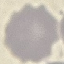

Summary:
  - Malaria status: uninfected
  - Stain: Giemsa
  - Image type: cell patch, automatically extracted from a larger field of view and resized to 64 × 64 pixels
  - Preparation: thin blood film
  - Capture: smartphone through the microscope eyepiece